Assess this cell for malaria.
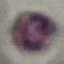
Uninfected.

Summary:
  - Image type: automatically extracted cell patch, resized to 64 × 64 pixels
  - Capture: smartphone camera at the microscope eyepiece
  - Preparation: thin blood film
  - Stain: Giemsa